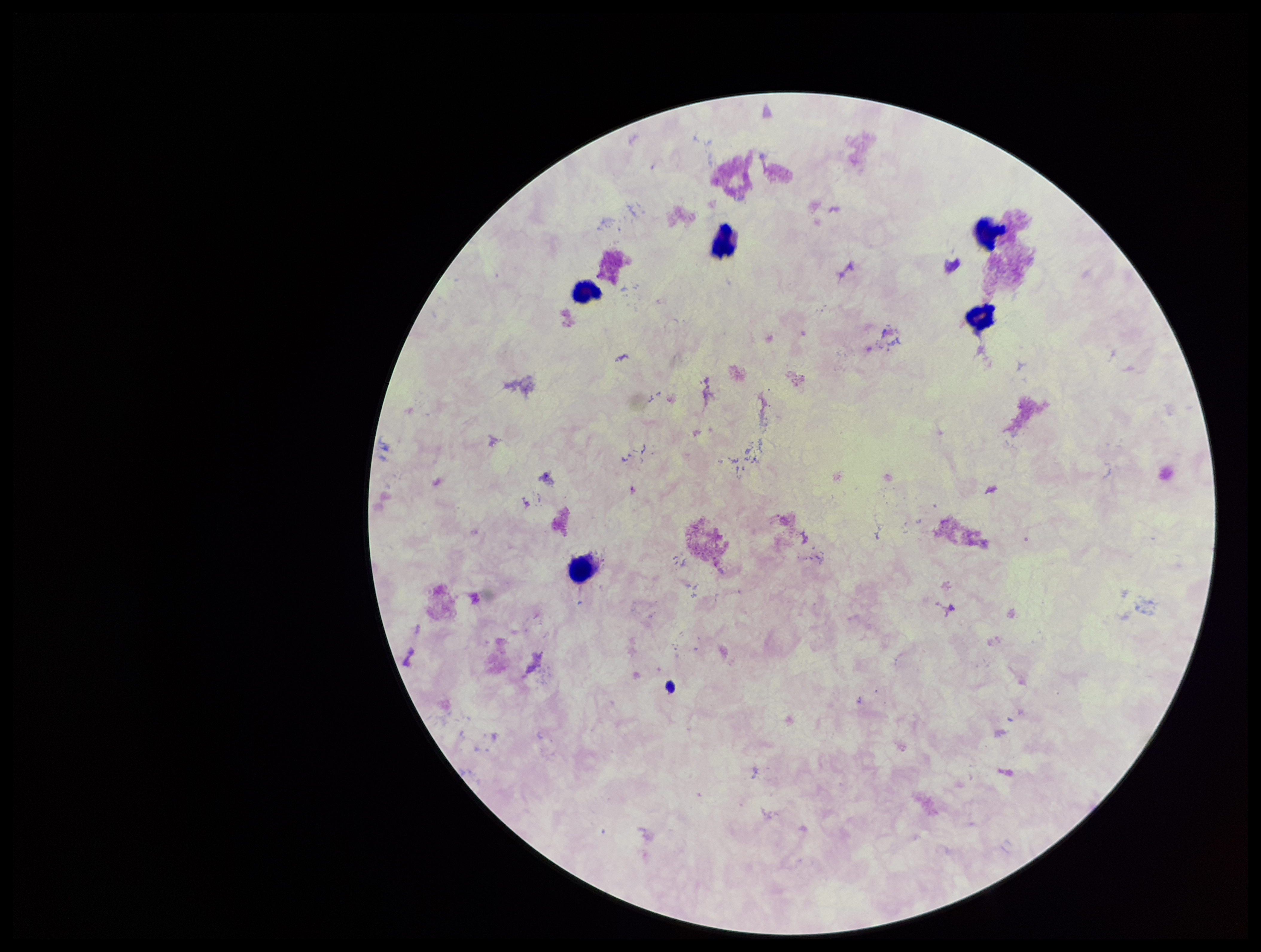
Summary:
  - Field of view: single
  - Image size: 1261×952 pixels
  - Preparation: thick blood smear
  - Stain: Giemsa
  - Parasite count: 0
  - Plasmodium parasites: none seen
  - Capture: smartphone photograph through the microscope eyepiece
  - Patient malaria status: negative
  - Leukocyte count: 5